Report the malaria status of this cell.
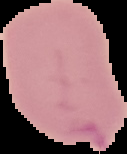
Uninfected.

Cell region segmented out of the field of view; the surrounding area is masked to black. Image is 127×154 pixels. From a thin blood film.